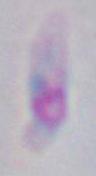
magnification = 1000x
identification = Toxoplasma gondii
modality = photomicrograph